Assess this cell for malaria.
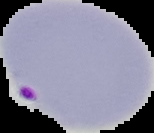
It is parasitized.

Summary:
  - Preparation: thin blood smear
  - Image type: cell region segmented out of the field of view; surrounding area masked to black
  - Image size: 154×133 pixels